Comment on the morphology of the red blood cells.
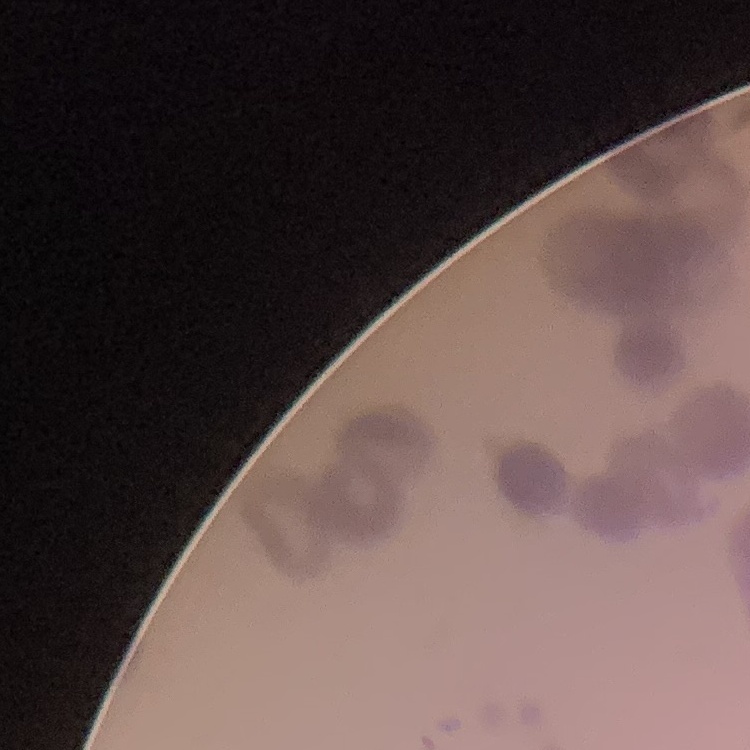
Rouleaux formation.

Summary:
  - Stain: Field's or Giemsa
  - Preparation: thin blood smear
  - Image type: one tile cut from a larger photomicrograph